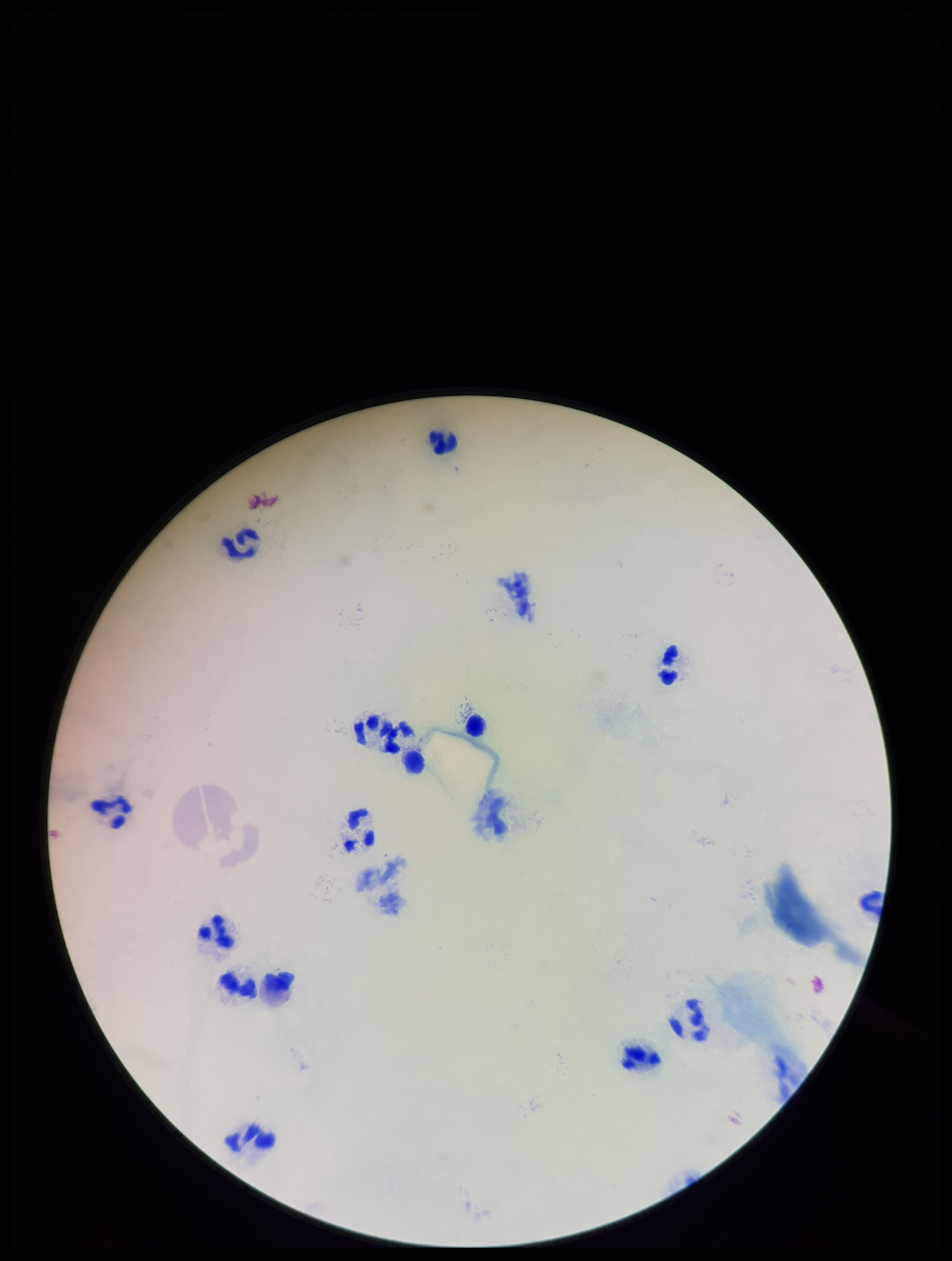

field of view = single
stain = Giemsa
patient malaria status = negative
parasite count = 0
preparation = thick smear
capture = smartphone photograph through the microscope eyepiece
leukocyte count = 15
Plasmodium parasites = none identified
image size = 952×1261 pixels